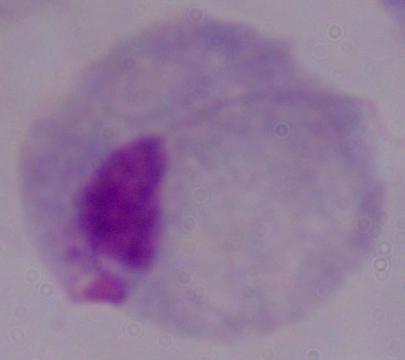
magnification: 1000x
modality: photomicrograph
identification: trichomonad